Name the parasite shown.
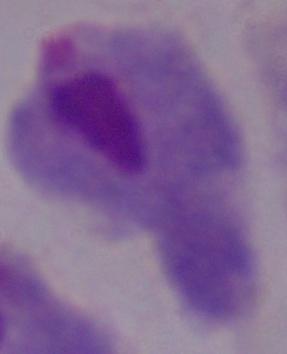

A trichomonad.

Summary:
  - Magnification: 1000x
  - Modality: photomicrograph